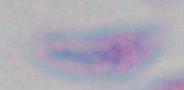

Summary:
  - Modality: photomicrograph
  - Magnification: 1000x
  - Identification: Toxoplasma gondii